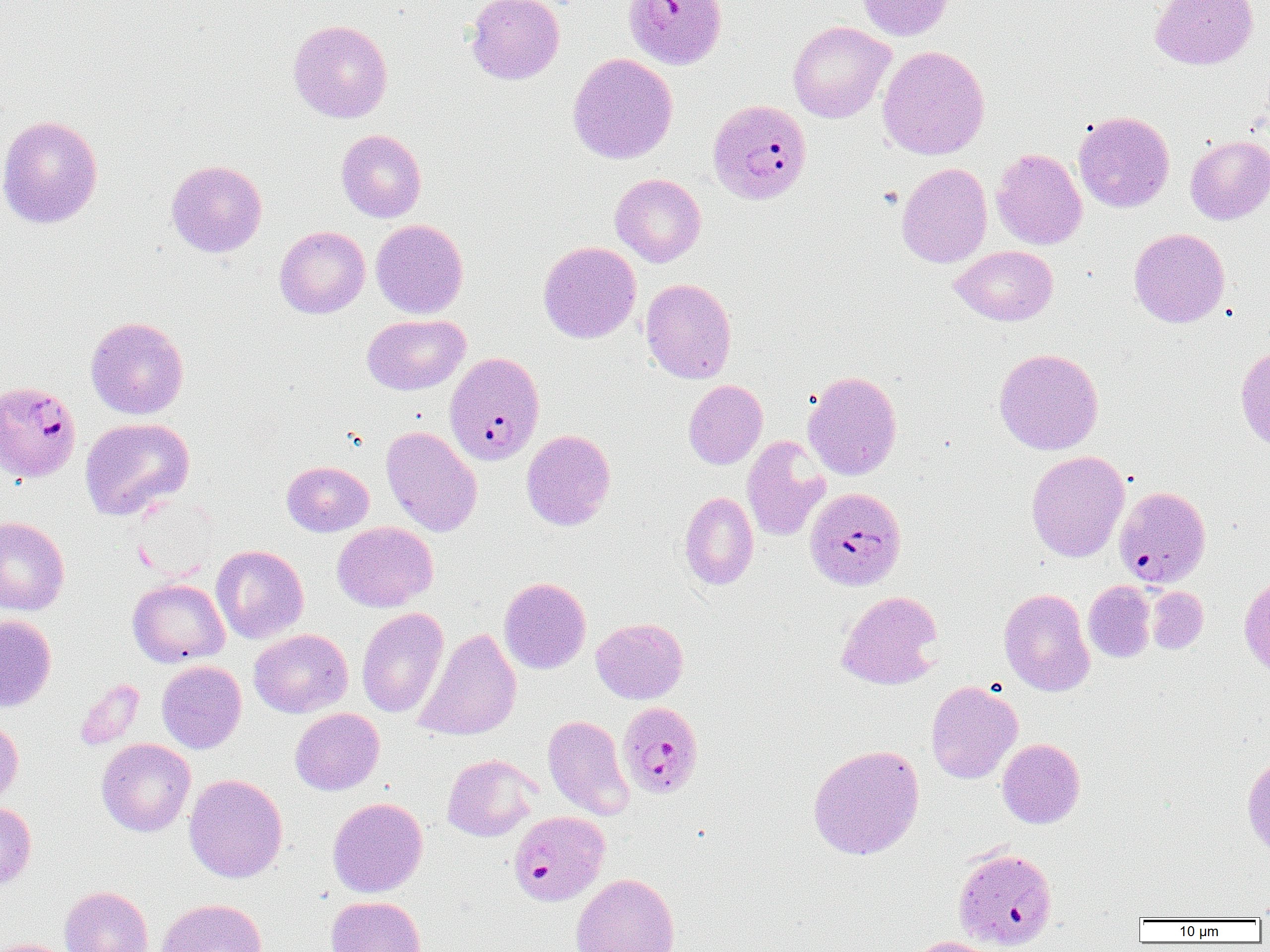

Summary:
  - Coordinate format: approximate bounding boxes as (x1,y1)-(x2,y2) corner pairs in pixels
  - Uninfected red blood cell locations: (465,0)-(565,84), (855,0)-(954,41), (1150,0)-(1258,70), (288,19)-(393,123), (788,21)-(895,123), (877,45)-(990,160), (567,53)-(678,164), (1074,111)-(1174,213), (0,114)-(103,229), (336,129)-(427,222), (1185,135)-(1270,224), (991,148)-(1087,250), (166,159)-(267,257), (896,162)-(993,268), (610,173)-(706,267), (371,219)-(468,318), (274,226)-(370,319), (1129,228)-(1230,328), (538,241)-(641,343), (951,245)-(1058,326), (640,278)-(737,383), (362,314)-(470,395), (85,316)-(189,419), (1235,344)-(1270,452), (994,348)-(1104,455), (802,370)-(902,480), (683,379)-(768,469), (80,417)-(195,521), (381,426)-(483,537), (521,429)-(616,530), (742,435)-(831,542), (1026,450)-(1130,563), (281,461)-(374,537), (679,491)-(758,590), (0,516)-(70,615), (332,521)-(438,612), (211,545)-(309,643), (1239,574)-(1270,680), (499,577)-(591,674), (128,578)-(230,667), (1083,581)-(1156,662), (1146,586)-(1208,654), (999,587)-(1095,696), (836,590)-(944,690), (356,607)-(449,718), (0,615)-(57,712), (591,617)-(689,704), (415,627)-(521,741), (249,628)-(353,718), (156,660)-(246,753), (74,679)-(144,749), (925,681)-(1022,784), (290,708)-(384,795), (542,714)-(634,820), (0,717)-(24,806), (97,738)-(195,837), (997,738)-(1085,829), (807,744)-(925,860), (442,754)-(539,841), (1242,754)-(1270,856), (184,773)-(288,882), (327,797)-(428,898), (0,801)-(36,889), (953,845)-(1058,950), (570,873)-(680,952), (59,885)-(154,952), (1254,893)-(1270,920), (326,896)-(427,952), (157,898)-(267,952), (907,936)-(1003,952), (0,938)-(79,952)
  - Plasmodium falciparum-infected red blood cell locations: (622,0)-(727,70), (707,98)-(812,205), (445,352)-(545,465), (0,380)-(82,484), (1115,485)-(1211,588), (805,487)-(906,590), (616,701)-(704,799), (510,810)-(610,908)
  - Slide-level diagnosis: Plasmodium falciparum
  - Modality: light microscopy
  - Image size: 1270×952 pixels
  - Preparation: thin blood smear
  - Field of view: one of a larger specimen
  - Magnification: 1000x